Point out each Plasmodium parasite.
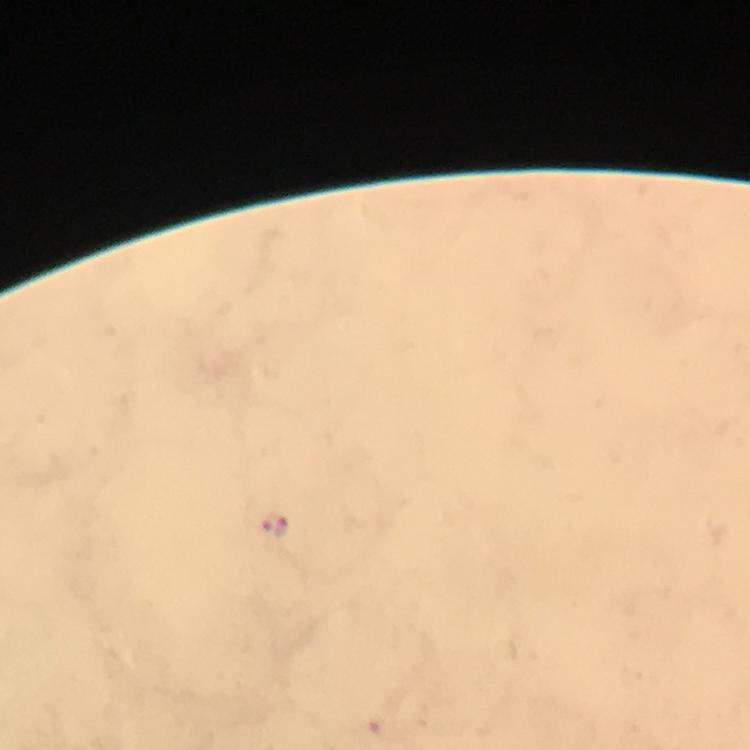

Approximate centers as [x, y] in pixels.
Plasmodium parasites: [274, 524].

Giemsa stain. 100x magnification. From a diagnostic examination for malaria. Thick smear. Image is 750×750 pixels. Cropped region of a single field of view. Immersion oil was used. Photographed through the microscope with a smartphone camera.